Locate every Plasmodium falciparum parasite and give its life-cycle stage, and locate every leukocyte and any debris.
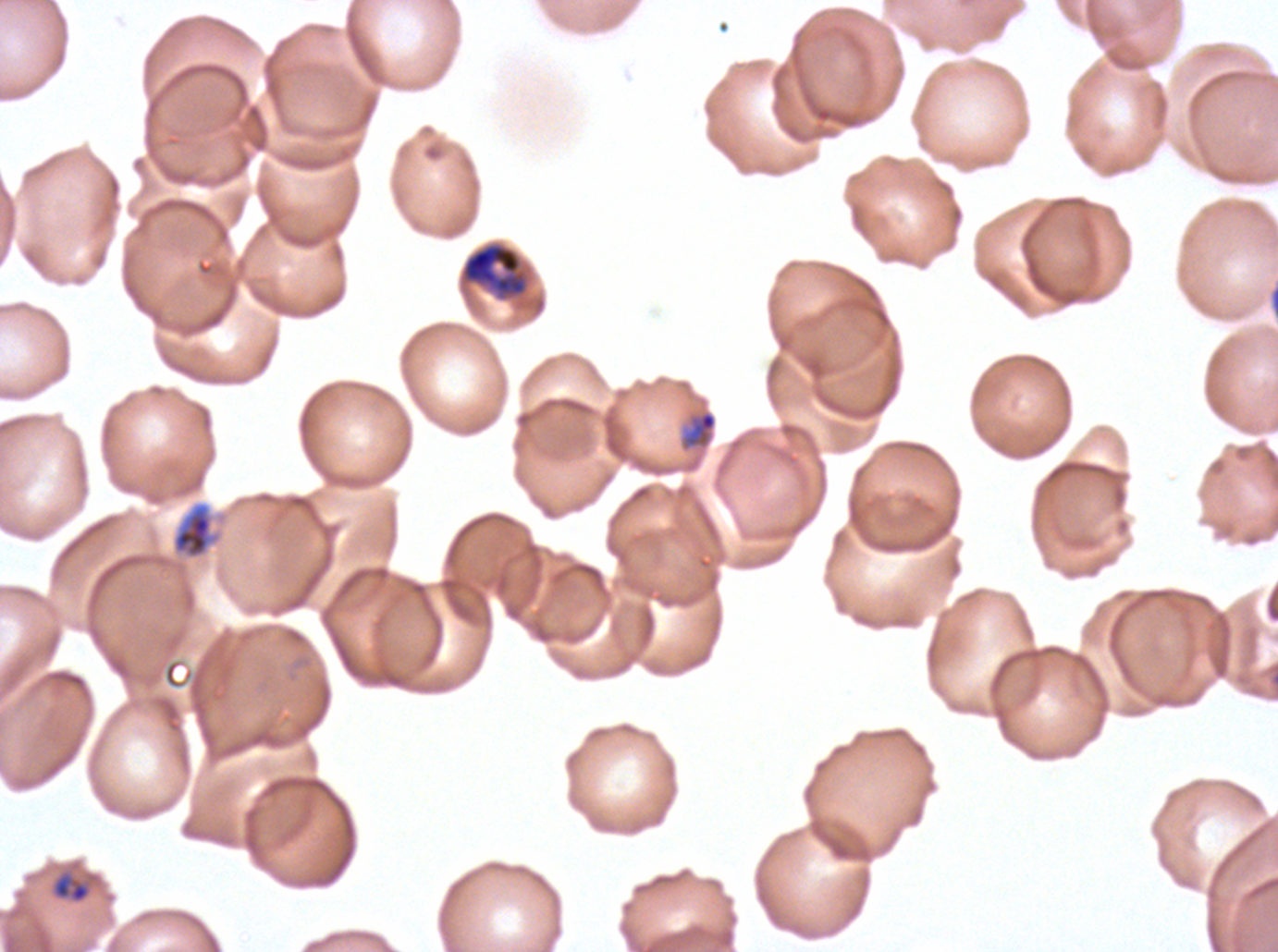

Approximate bounding boxes as [x1, y1, x2, y2] in pixels.
Late-ring/early-trophozoite forms: [681, 409, 718, 451], [53, 876, 90, 903].
Mid trophozoites: [171, 502, 219, 559].
Late trophozoites: [461, 242, 528, 298].
No rings, early schizonts, late schizonts, segmenters, gametocytes, leukocytes, or debris observed.

Image is 1278×952 pixels. Life-cycle stages observed: late-ring/early-trophozoite, mid trophozoite, late trophozoite. Giemsa-stained preparation. Plasmodium falciparum from a patient in The Gambia, cultured ex vivo for 24 to 48 hours. One sub-image of a larger composite. Thin blood film.